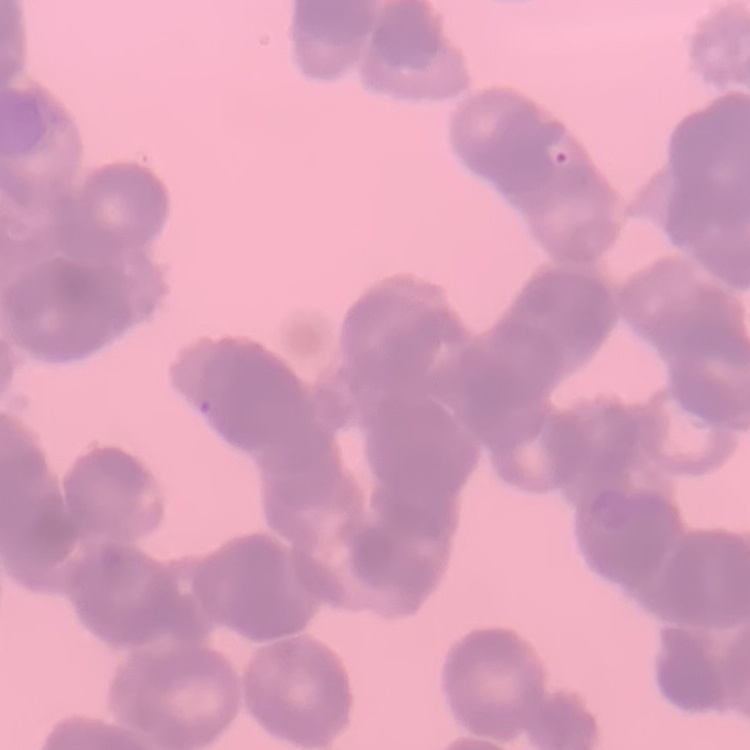
Summary:
  - Red blood cell morphology: rouleaux formation
  - Image type: square crop of a larger photomicrograph
  - Stain: Field's or Giemsa
  - Preparation: thin blood film